Give the extent of all uninfected red blood cells.
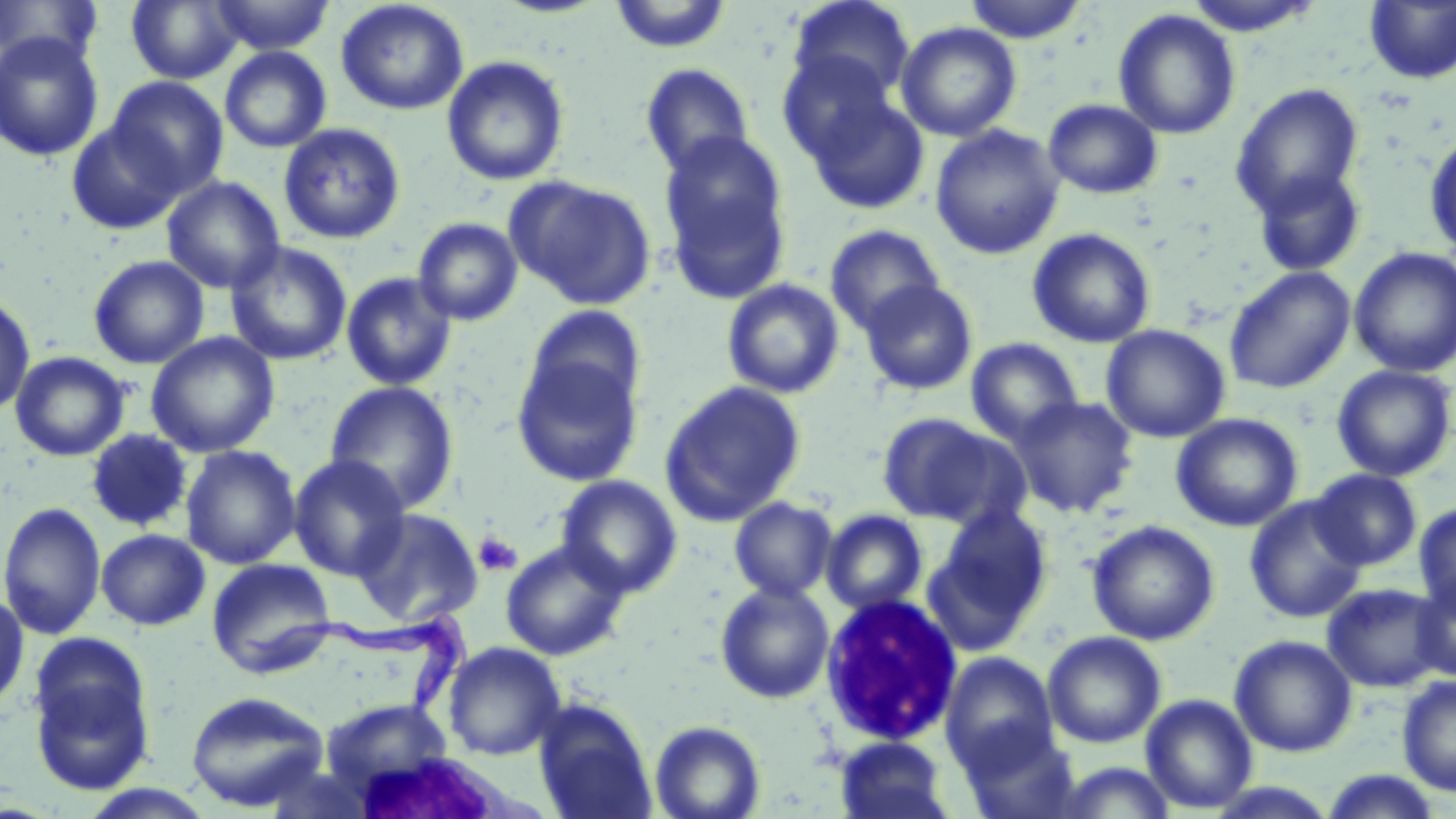
Approximate bounding boxes as (x1,y1)-(x2,y2) corner pairs in pixels.
Uninfected red blood cells: (0,0)-(102,68), (126,0)-(244,84), (210,0)-(334,56), (335,0)-(469,116), (961,0)-(1090,44), (1182,0)-(1326,36), (609,1)-(733,54), (787,1)-(914,106), (1364,1)-(1456,85), (1113,9)-(1241,140), (896,22)-(1022,142), (0,32)-(104,162), (219,46)-(332,154), (777,49)-(899,164), (442,55)-(569,187), (640,63)-(756,179), (105,76)-(229,198), (1230,83)-(1364,218), (803,89)-(929,215), (1043,98)-(1163,199), (67,121)-(185,235), (279,124)-(405,244), (930,125)-(1065,260), (1424,130)-(1456,259), (658,136)-(792,305), (1251,165)-(1366,278), (162,176)-(285,294), (507,176)-(656,310), (412,217)-(523,326), (824,224)-(945,335), (1027,228)-(1156,348), (225,241)-(352,365), (1349,247)-(1456,378), (88,255)-(210,369), (1224,266)-(1356,395), (341,272)-(457,391), (722,279)-(845,399), (859,280)-(978,396), (0,294)-(36,416), (525,305)-(647,416), (1101,324)-(1230,443), (145,332)-(280,458), (965,337)-(1085,446), (10,351)-(130,461), (512,356)-(643,487), (1331,364)-(1454,482), (324,380)-(460,515), (659,381)-(806,525), (1010,396)-(1139,517), (877,412)-(1015,527), (1171,413)-(1304,532), (86,428)-(192,532), (180,445)-(301,570), (288,454)-(410,581), (1310,469)-(1422,571), (556,475)-(683,597), (1243,495)-(1368,623), (729,497)-(838,602), (0,501)-(106,640), (1414,502)-(1456,617), (351,507)-(483,627), (936,507)-(1051,628), (821,510)-(927,614), (1087,520)-(1220,645), (96,528)-(210,631), (500,540)-(631,661), (922,551)-(1037,657), (206,559)-(336,678), (1413,576)-(1456,681), (715,581)-(834,704), (1321,583)-(1449,693), (0,590)-(29,714), (1042,630)-(1167,748), (1229,634)-(1357,757), (443,642)-(565,760), (29,648)-(156,797), (940,652)-(1058,771), (1396,674)-(1456,796), (186,691)-(329,812), (1140,693)-(1258,813), (532,698)-(657,819), (320,700)-(454,795), (650,720)-(766,819), (959,724)-(1082,819), (835,736)-(955,819), (1057,761)-(1178,819), (1318,770)-(1444,818), (77,785)-(218,818).

Trypanosoma brucei locations: (245,608)-(474,721). White blood cell locations: (818,592)-(963,746), (357,754)-(549,819). Platelet locations: (476,533)-(521,575). Slide-level diagnosis: Trypanosoma brucei. One field of a larger specimen. Light microscopy. Captured at 1000x magnification. May-Grünwald-Giemsa-stained preparation. Image is 1456×819 pixels. Thin blood film.